Assess the morphology of the erythrocytes.
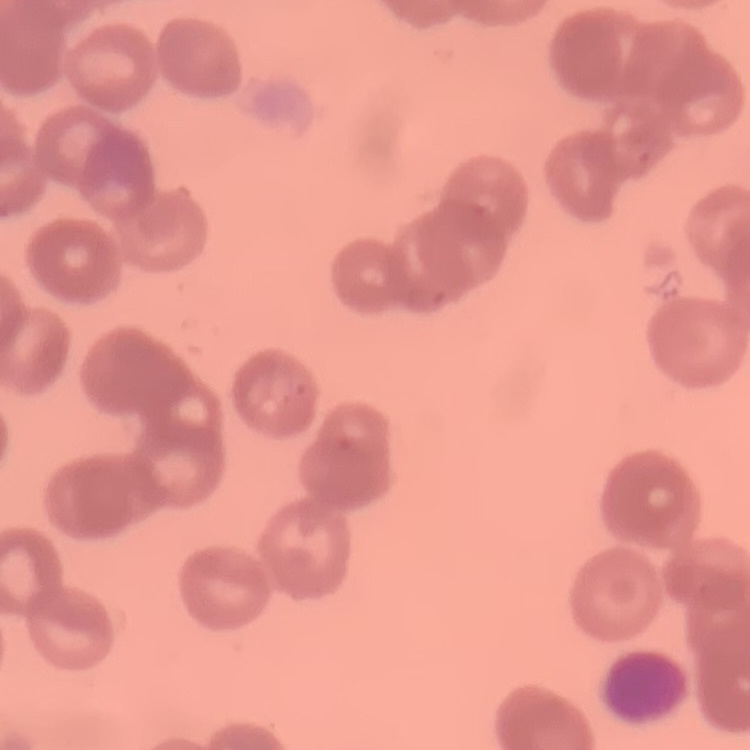
They show rouleaux formation.

Field's or Giemsa stain. Thin blood film. Square crop of a larger photomicrograph.